Assess this cell for malaria.
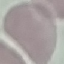

It is uninfected.

Summary:
  - Stain: Giemsa
  - Image type: automatically extracted cell patch, resized to 64 × 64 pixels
  - Capture: smartphone through the microscope eyepiece
  - Preparation: thin blood smear